Assess this cell for malaria.
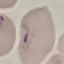

It is parasitized.

Giemsa-stained preparation. Acquired by smartphone through the microscope eyepiece. Automatically extracted cell patch, resized to 64 × 64 pixels. Thin smear of blood.